Report the malaria status of this cell.
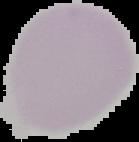

It is uninfected.

The area outside the segmented cell region is set to black. Image is 139×142 pixels. From a thin blood film.